Assess the morphology of the red blood cells.
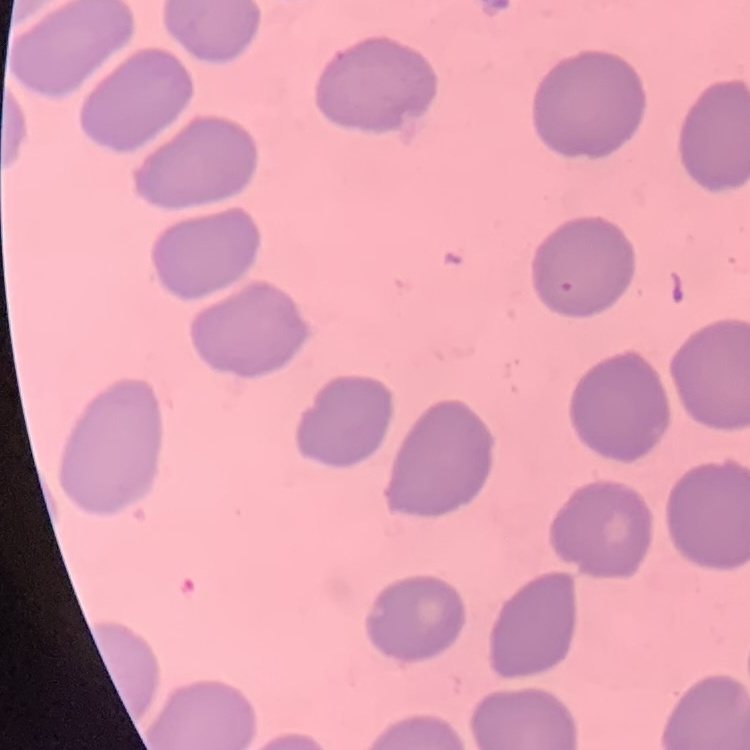

They show no rouleaux formation.

One tile cut from a larger photomicrograph. Field's or Giemsa stain. Thin blood smear.